Comment on the morphology of the erythrocytes.
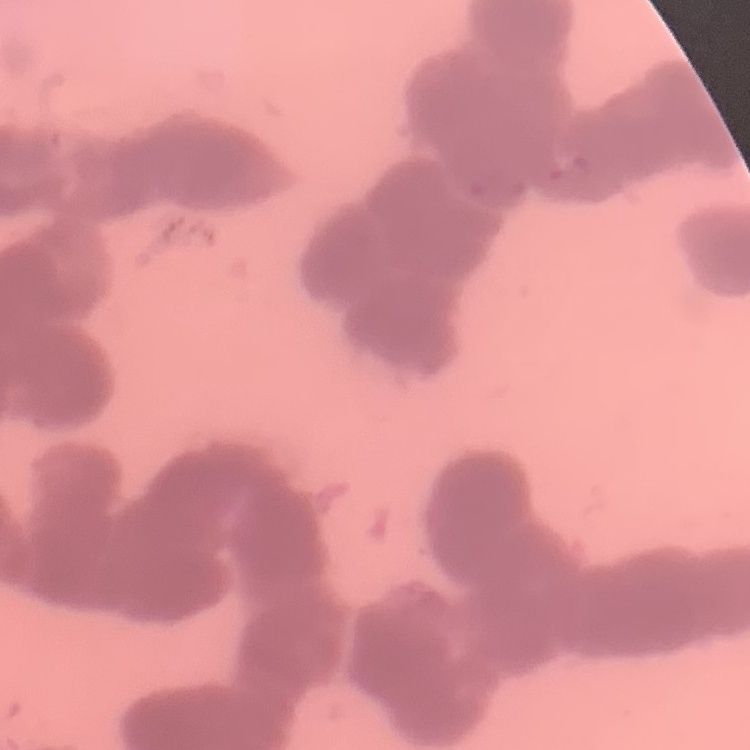

Rouleaux formation.

Square crop of a larger photomicrograph. Field's or Giemsa stain. Thin blood smear.